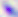
modality: photomicrograph
magnification: 400x
identification: Toxoplasma gondii